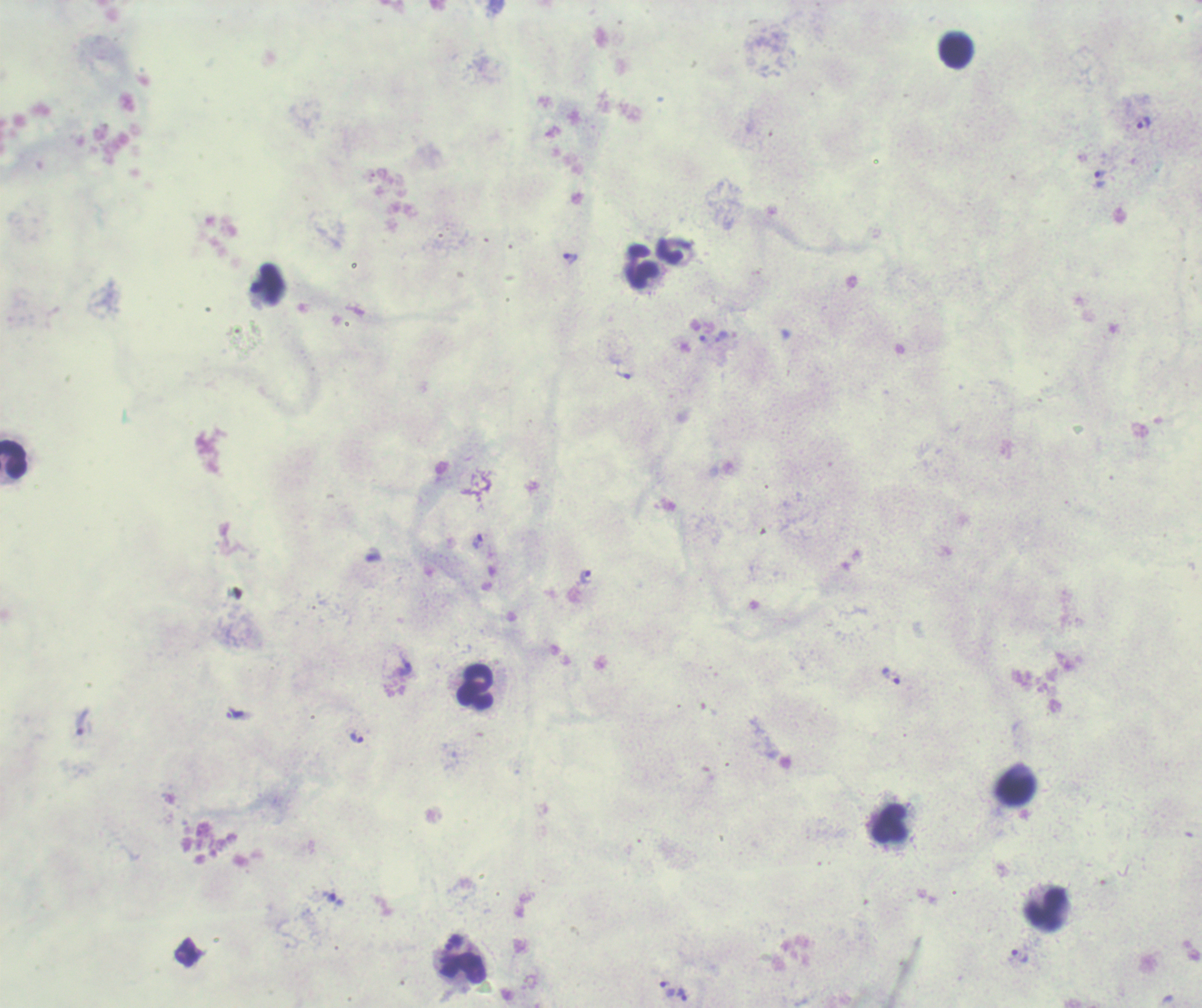

Approximate centers as [x, y] in pixels.
Summary:
  - Leukocyte locations: [955, 51], [642, 268], [13, 460], [475, 687], [1018, 788], [891, 822], [1045, 911], [461, 968]
  - Trophozoite locations: [1143, 122], [1100, 178], [570, 258], [266, 284], [721, 335], [622, 375], [477, 541], [586, 576], [404, 667], [895, 677], [235, 713], [82, 721], [356, 737], [454, 942], [1020, 955], [667, 990], [681, 993]
  - Background quality: poor
  - Preparation: thick blood smear
  - Field of view: one from this slide
  - Stain: Romanowsky
  - Image size: 1202×1008 pixels
  - Result: positive for Plasmodium parasites
  - Context: previously used in a real diagnosis
  - Magnification: 100x